Assess this cell for malaria.
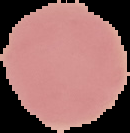
It is uninfected.

Summary:
  - Image type: segmented cell region with the area outside set to black
  - Image size: 130×133 pixels
  - Preparation: thin blood film